Outline each uninfected red blood cell.
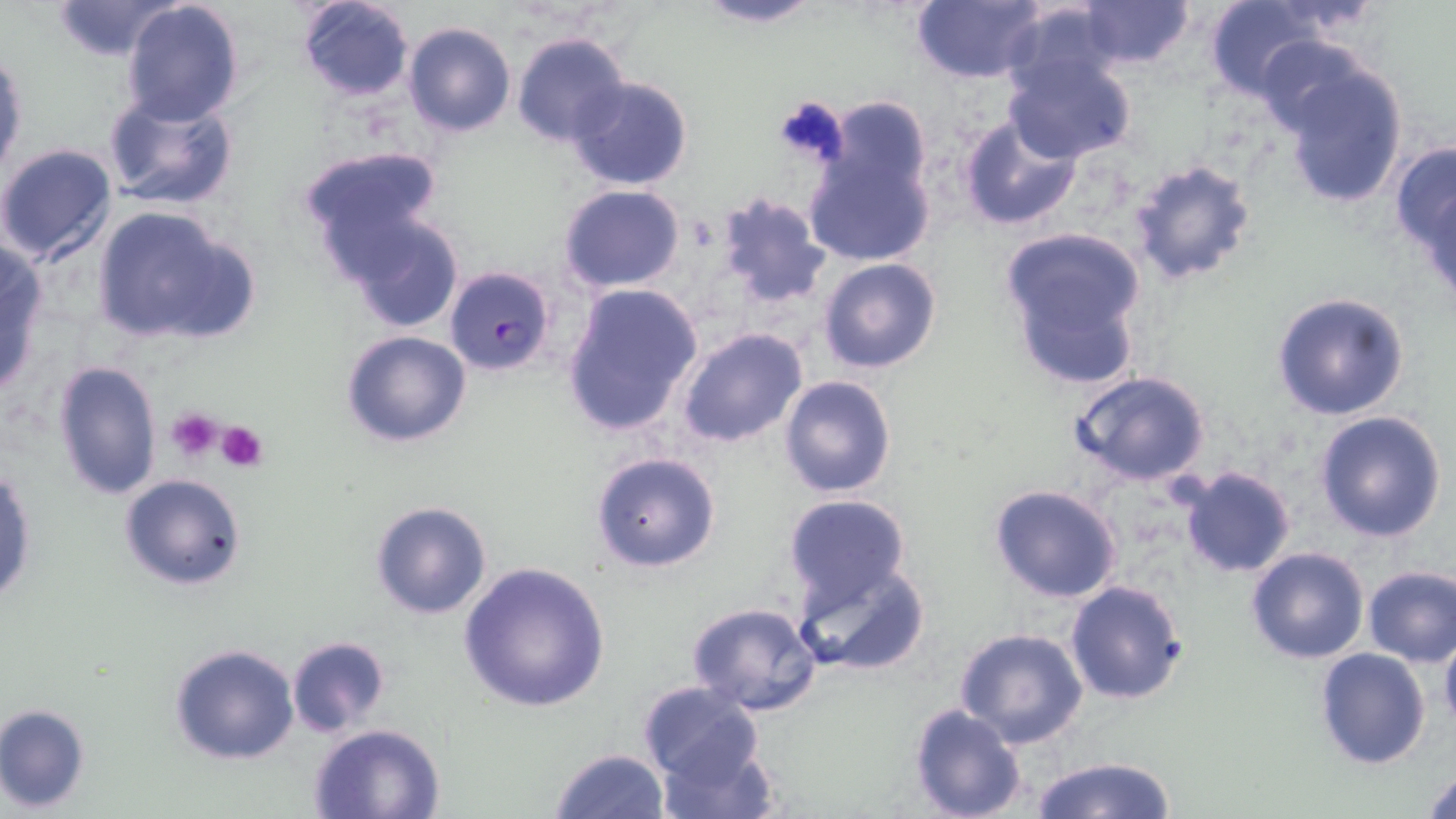
Approximate bounding boxes as (x1, y1, x2, y2) in pixels.
Uninfected red blood cells: (51, 0, 185, 60), (119, 0, 246, 126), (295, 0, 416, 101), (689, 0, 829, 29), (910, 0, 1049, 84), (1202, 0, 1327, 104), (1078, 1, 1194, 71), (1000, 3, 1125, 100), (403, 21, 515, 137), (512, 32, 632, 148), (1249, 33, 1379, 139), (1, 45, 27, 182), (1000, 49, 1138, 166), (1274, 58, 1411, 210), (565, 74, 693, 190), (102, 90, 240, 209), (955, 113, 1083, 233), (801, 124, 937, 271), (1392, 142, 1456, 276), (0, 143, 119, 268), (297, 146, 446, 278), (1127, 156, 1259, 285), (558, 184, 687, 295), (711, 191, 828, 309), (90, 204, 256, 348), (339, 209, 466, 333), (1000, 229, 1152, 389), (0, 240, 50, 395), (818, 257, 942, 372), (561, 282, 703, 439), (1271, 292, 1410, 421), (677, 327, 807, 448), (340, 329, 472, 447), (52, 358, 163, 501), (1069, 371, 1213, 489), (779, 374, 895, 498), (1313, 410, 1447, 542), (590, 450, 722, 573), (1, 463, 36, 609), (1176, 466, 1296, 580), (119, 473, 248, 593), (988, 485, 1124, 604), (781, 494, 911, 611), (370, 500, 493, 620), (1245, 547, 1370, 664), (793, 558, 932, 677), (457, 560, 609, 712), (1362, 565, 1456, 666), (1064, 579, 1187, 706), (687, 600, 821, 716), (955, 627, 1089, 749), (1439, 631, 1456, 736), (286, 637, 390, 735), (168, 643, 300, 765), (1314, 647, 1431, 769), (636, 680, 766, 789), (0, 703, 90, 812), (907, 704, 1029, 819), (308, 723, 447, 818), (654, 734, 782, 819), (550, 746, 671, 819), (1026, 756, 1182, 819), (1422, 764, 1456, 817).

Plasmodium falciparum-infected red blood cell locations = approximate bounding boxes as (x1, y1, x2, y2) in pixels: (445, 266, 555, 374)
slide-level diagnosis = Plasmodium falciparum
magnification = 1000x
field of view = one of a larger specimen
image size = 1456×819 pixels
platelet locations = approximate bounding boxes as (x1, y1, x2, y2) in pixels: (771, 95, 852, 170), (165, 407, 226, 465), (216, 420, 268, 472)
preparation = thin blood film
stain = May-Grünwald-Giemsa
modality = optical microscopy